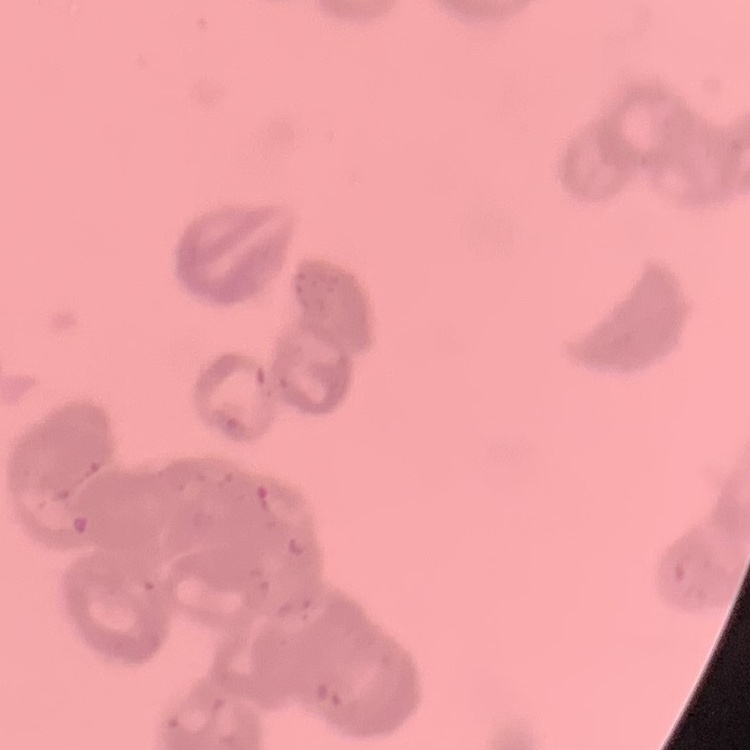

The erythrocytes exhibit rouleaux formation. Square crop of a larger photomicrograph. Thin blood smear. Field's or Giemsa stain.